Report the malaria status of this cell.
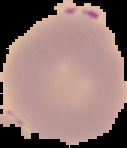

It is uninfected.

Summary:
  - Preparation: thin blood film
  - Image size: 127×148 pixels
  - Image type: segmented cell region on a black background